Assess the morphology of the erythrocytes.
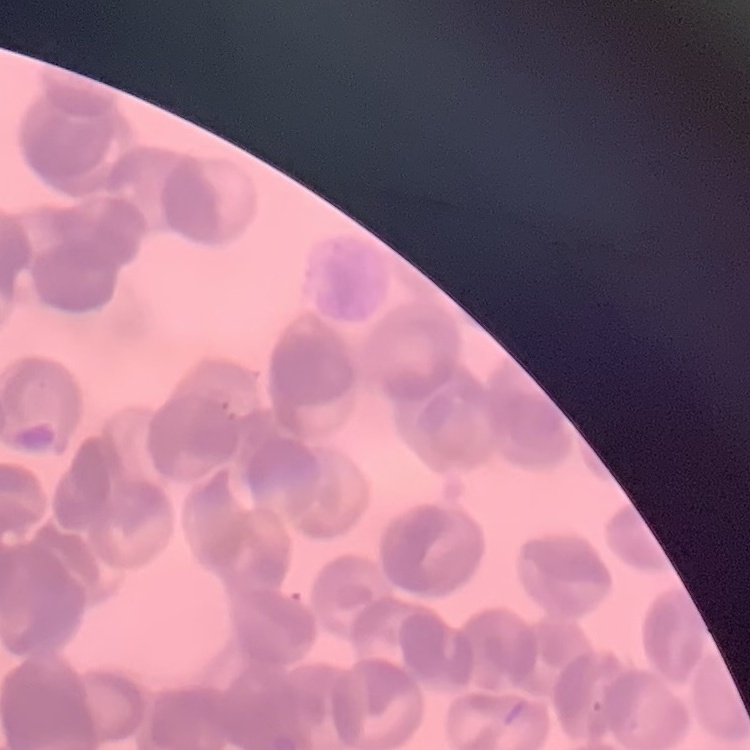

They show rouleaux formation.

One tile cut from a larger photomicrograph. Field's or Giemsa stain. Thin blood film.